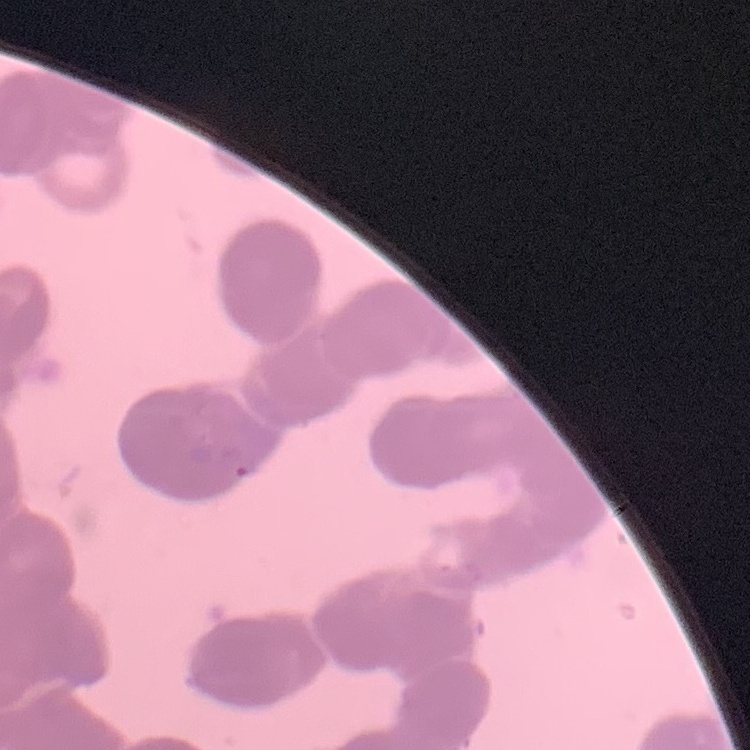
erythrocyte morphology = rouleaux formation
stain = Field's or Giemsa
image type = square crop of a larger photomicrograph
preparation = thin peripheral smear